Report the malaria status.
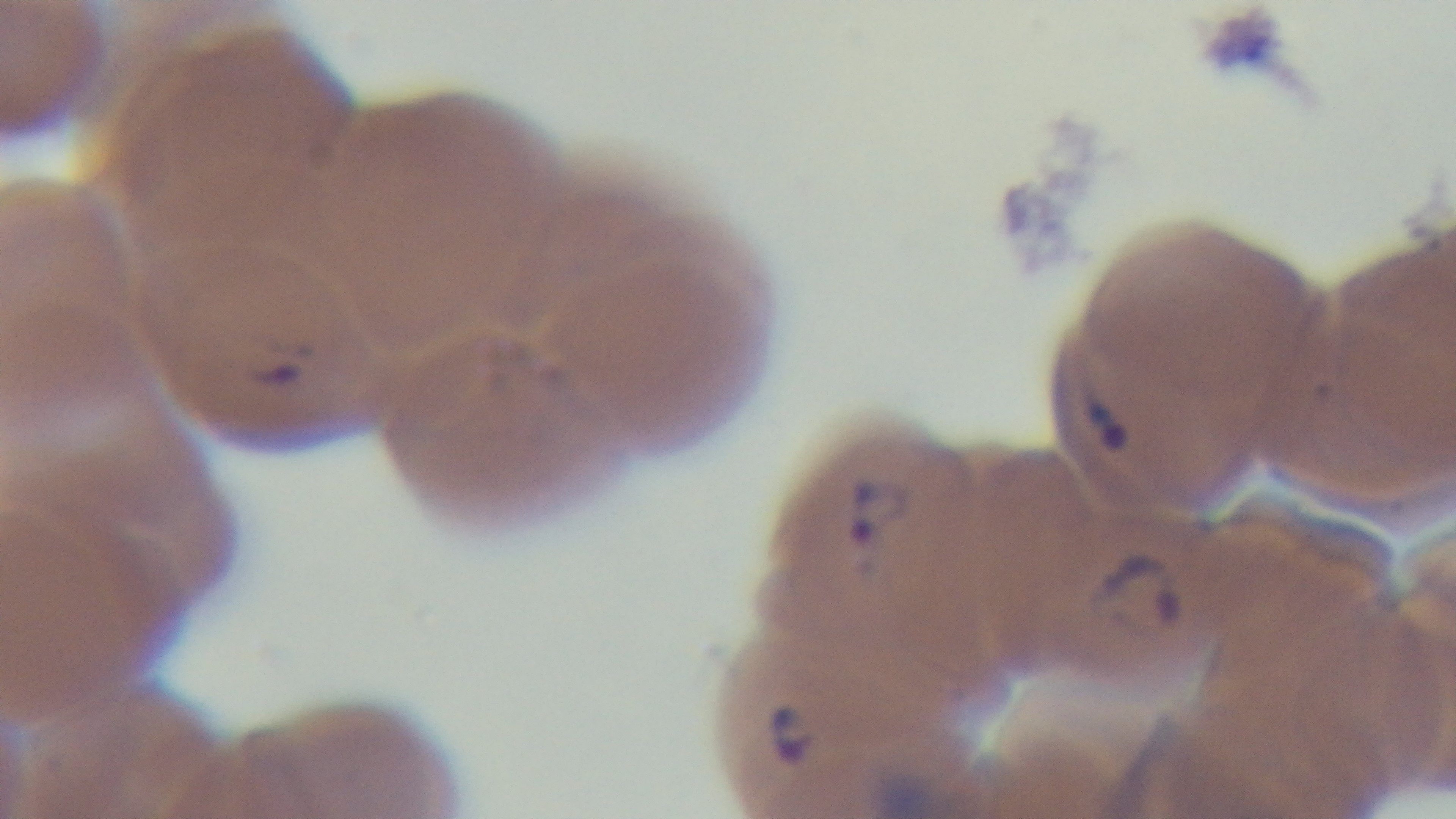

Infected.

Summary:
  - Modality: light microscopy
  - Capture: mounted 4K digital camera
  - Preparation: thin smear
  - Stain: Giemsa
  - Field of view: single
  - Objective: 100x oil immersion